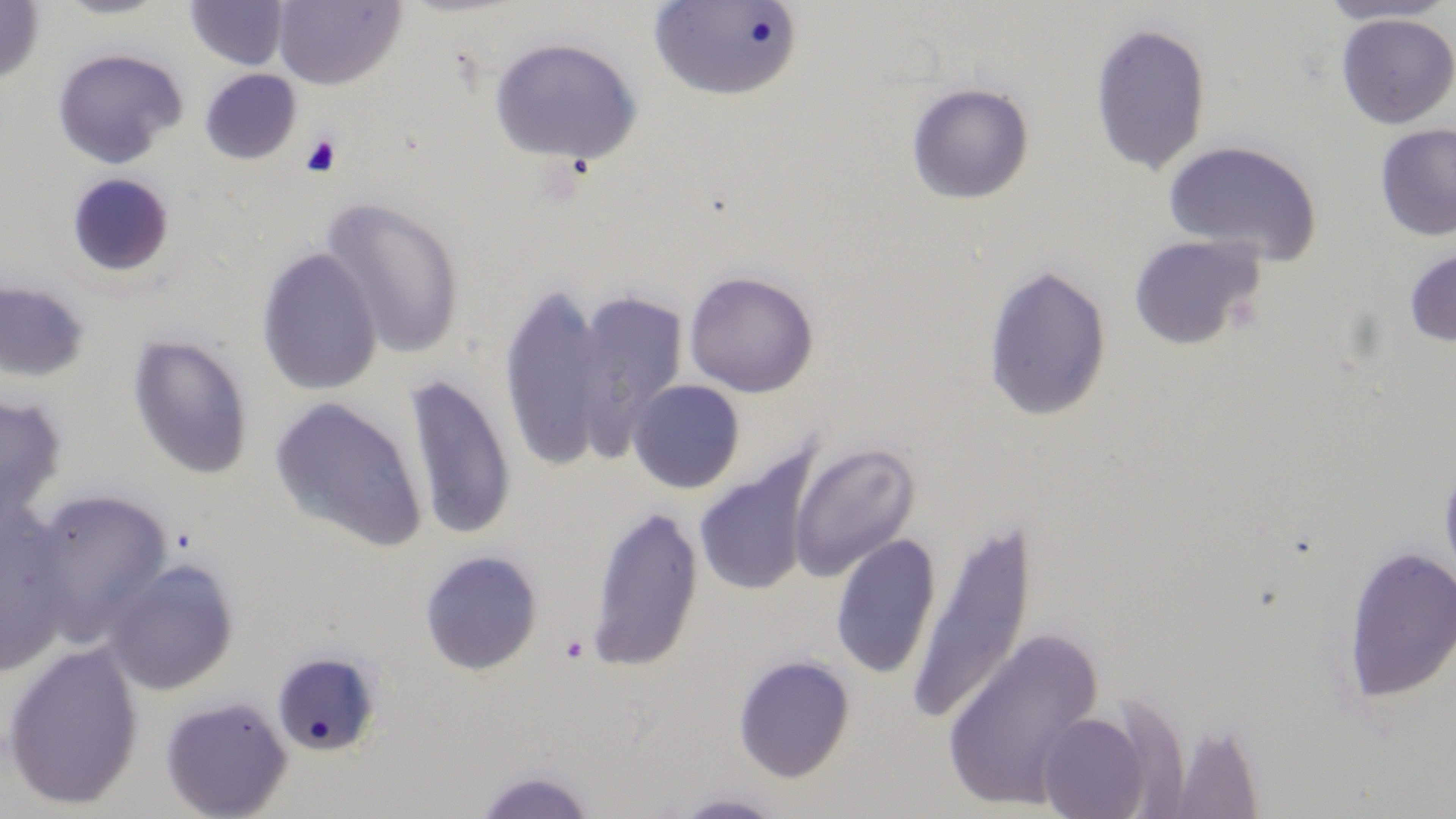
Approximate bounding boxes as named x1/y1/x2/y2 corners in pixels. Uninfected red blood cell locations: (x1=0, y1=0, x2=44, y2=86), (x1=52, y1=0, x2=174, y2=20), (x1=272, y1=0, x2=406, y2=90), (x1=1315, y1=0, x2=1456, y2=26), (x1=184, y1=1, x2=289, y2=70), (x1=650, y1=1, x2=803, y2=101), (x1=1334, y1=13, x2=1456, y2=129), (x1=1088, y1=21, x2=1212, y2=177), (x1=488, y1=36, x2=643, y2=168), (x1=51, y1=46, x2=188, y2=168), (x1=199, y1=68, x2=302, y2=164), (x1=905, y1=82, x2=1035, y2=205), (x1=1374, y1=123, x2=1456, y2=242), (x1=1162, y1=139, x2=1323, y2=264), (x1=65, y1=172, x2=176, y2=279), (x1=321, y1=196, x2=466, y2=359), (x1=1127, y1=234, x2=1267, y2=351), (x1=256, y1=247, x2=382, y2=396), (x1=1403, y1=247, x2=1456, y2=347), (x1=981, y1=263, x2=1112, y2=424), (x1=683, y1=270, x2=819, y2=398), (x1=0, y1=279, x2=93, y2=384), (x1=498, y1=284, x2=613, y2=474), (x1=567, y1=290, x2=689, y2=460), (x1=126, y1=334, x2=254, y2=479), (x1=403, y1=372, x2=517, y2=542), (x1=627, y1=380, x2=745, y2=494), (x1=0, y1=393, x2=68, y2=525), (x1=269, y1=396, x2=427, y2=552), (x1=789, y1=442, x2=921, y2=582), (x1=1438, y1=453, x2=1456, y2=592), (x1=694, y1=459, x2=815, y2=597), (x1=26, y1=488, x2=171, y2=643), (x1=585, y1=505, x2=705, y2=672), (x1=906, y1=513, x2=1038, y2=729), (x1=0, y1=514, x2=73, y2=675), (x1=829, y1=533, x2=942, y2=680), (x1=1340, y1=545, x2=1456, y2=704), (x1=418, y1=550, x2=544, y2=676), (x1=102, y1=557, x2=240, y2=695), (x1=942, y1=627, x2=1105, y2=811), (x1=1, y1=642, x2=145, y2=811), (x1=270, y1=649, x2=383, y2=757), (x1=732, y1=654, x2=855, y2=783), (x1=159, y1=695, x2=293, y2=819), (x1=1037, y1=711, x2=1152, y2=819), (x1=1161, y1=721, x2=1267, y2=819), (x1=470, y1=767, x2=597, y2=818), (x1=668, y1=791, x2=787, y2=818). Platelet locations: (x1=300, y1=134, x2=342, y2=178), (x1=560, y1=634, x2=589, y2=663). Slide-level diagnosis: no evidence of blood parasites. One field of a larger specimen. 1000x magnification. Optical microscopy. May-Grünwald-Giemsa-stained preparation. Image is 1456×819 pixels. Thin blood smear.